Assess this cell for malaria.
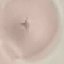
It is uninfected.

Giemsa stain. Photographed with a smartphone camera at the microscope eyepiece. Cell patch, automatically extracted from a larger field of view and resized to 64 × 64 pixels. Thin blood film.